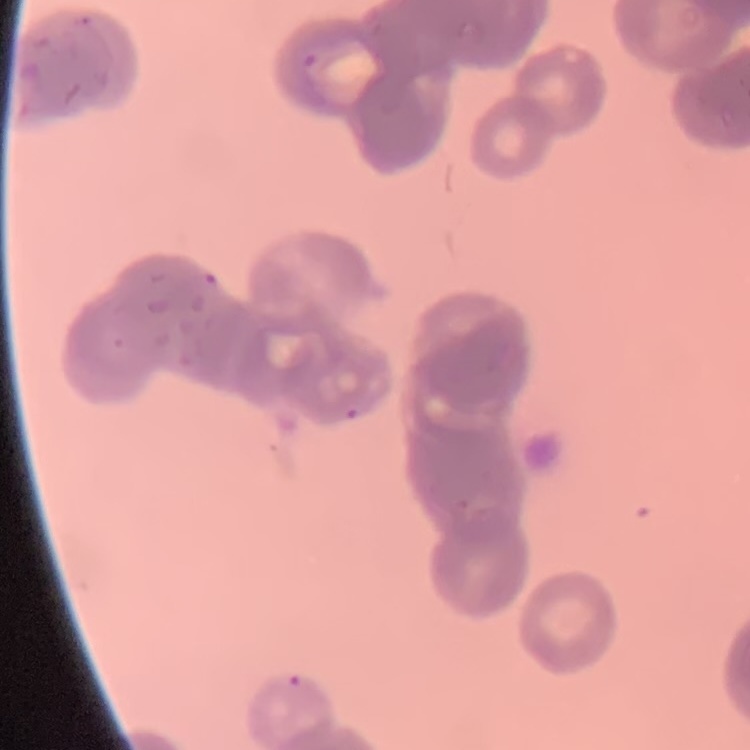

Summary:
  - Erythrocyte morphology: rouleaux formation
  - Image type: square crop of a larger photomicrograph
  - Stain: Field's or Giemsa
  - Preparation: thin blood film